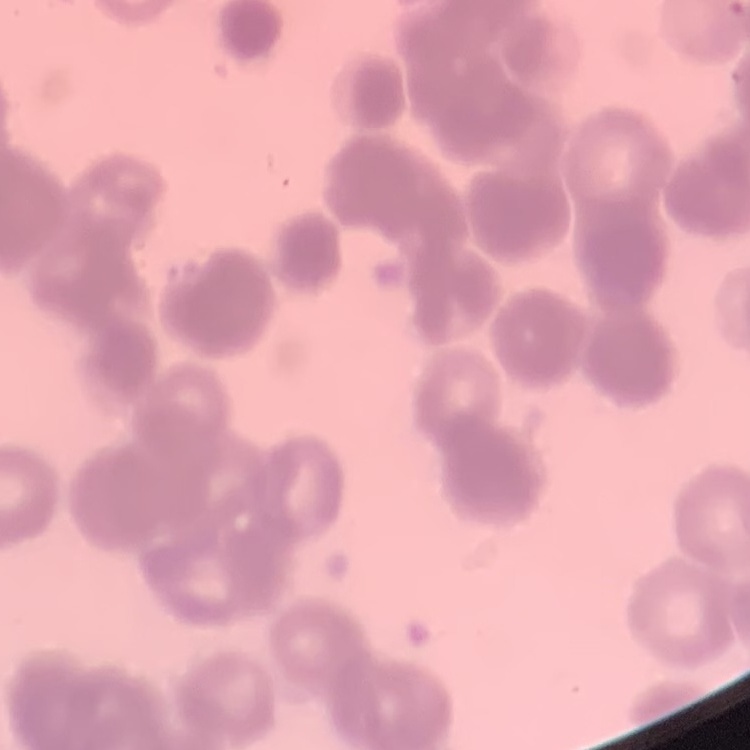

Summary:
  - Red blood cell morphology: rouleaux formation
  - Stain: Field's or Giemsa
  - Preparation: thin peripheral smear
  - Image type: square crop of a larger photomicrograph